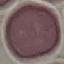
result = no malaria parasites seen
image type = automatically extracted cell patch, resized to 64 × 64 pixels
preparation = thin blood smear
capture = smartphone through the microscope eyepiece
stain = Giemsa